State which parasite is depicted.
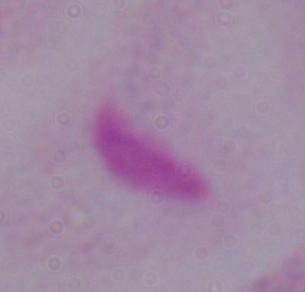

This is a trichomonad.

{
  "magnification": "1000x",
  "modality": "micrograph"
}